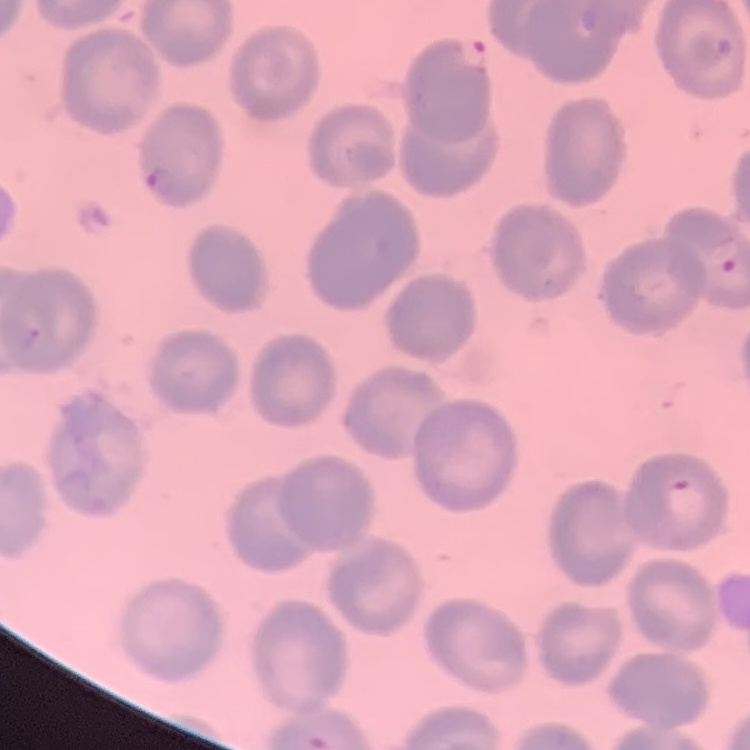 The red blood cells exhibit no rouleaux formation. One tile cut from a larger photomicrograph. Field's or Giemsa stain. Thin peripheral smear.